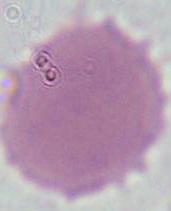
Micrograph. 1000x magnification. An erythrocyte is shown.